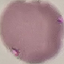

malaria status = uninfected
image type = automatically extracted cell patch, resized to 64 × 64 pixels
preparation = thin blood film
capture = smartphone through the microscope eyepiece
stain = Giemsa